Comment on the morphology of the erythrocytes.
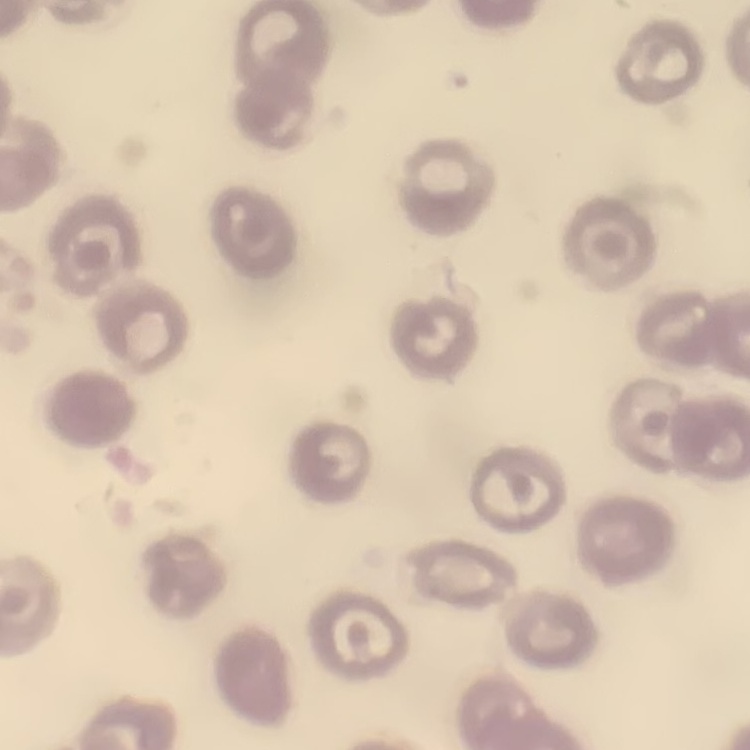
No rouleaux formation.

image_type: one tile cut from a larger photomicrograph
preparation: thin blood film
stain: Field's or Giemsa